Report the malaria status of this cell.
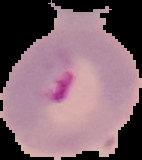
It is parasitized.

Image is 142×160 pixels. From a thin blood smear. Cell region segmented out of the field of view; the surrounding area is masked to black.